Comment on the morphology of the erythrocytes.
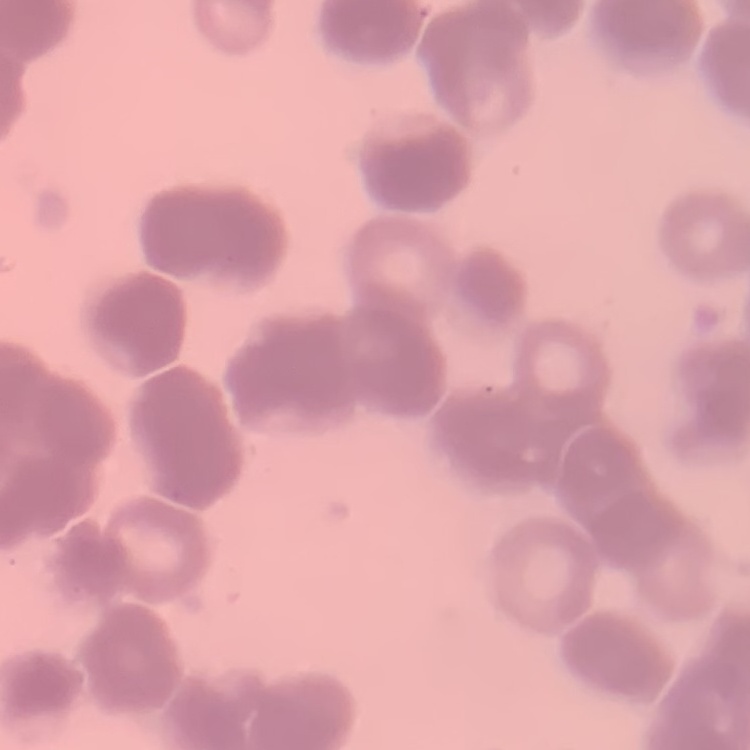
They show rouleaux formation.

Square crop of a larger photomicrograph. Thin blood smear. Field's or Giemsa stain.